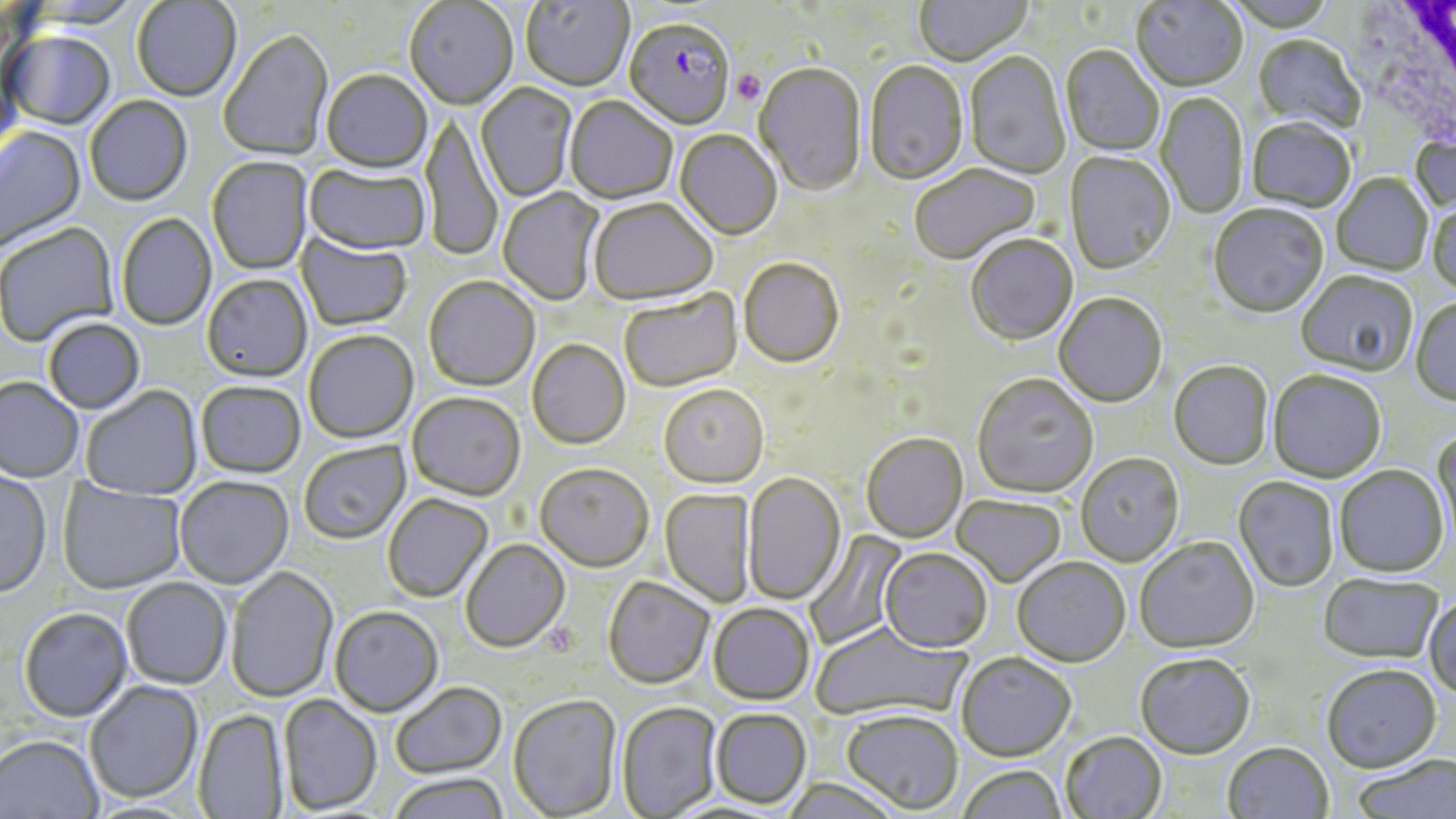

Approximate bounding boxes as named x1/y1/x2/y2 corners in pixels. White blood cell locations: (x1=1356, y1=0, x2=1456, y2=160). Plasmodium falciparum-infected red blood cell locations: (x1=624, y1=19, x2=735, y2=133). Uninfected red blood cell locations: (x1=521, y1=0, x2=633, y2=93), (x1=915, y1=0, x2=1032, y2=68), (x1=1131, y1=0, x2=1247, y2=93), (x1=132, y1=1, x2=242, y2=103), (x1=405, y1=1, x2=518, y2=111), (x1=218, y1=30, x2=334, y2=163), (x1=2, y1=32, x2=116, y2=132), (x1=1252, y1=36, x2=1365, y2=137), (x1=1061, y1=46, x2=1164, y2=157), (x1=964, y1=53, x2=1070, y2=180), (x1=864, y1=62, x2=968, y2=186), (x1=753, y1=64, x2=867, y2=198), (x1=321, y1=72, x2=433, y2=175), (x1=476, y1=84, x2=577, y2=203), (x1=1156, y1=92, x2=1248, y2=219), (x1=85, y1=97, x2=193, y2=208), (x1=565, y1=97, x2=677, y2=205), (x1=421, y1=112, x2=503, y2=263), (x1=1247, y1=120, x2=1355, y2=214), (x1=0, y1=125, x2=87, y2=255), (x1=674, y1=131, x2=782, y2=241), (x1=1410, y1=132, x2=1456, y2=216), (x1=1064, y1=152, x2=1175, y2=276), (x1=207, y1=157, x2=313, y2=276), (x1=304, y1=164, x2=431, y2=257), (x1=910, y1=165, x2=1041, y2=266), (x1=1332, y1=174, x2=1432, y2=276), (x1=497, y1=187, x2=605, y2=306), (x1=588, y1=199, x2=718, y2=308), (x1=1428, y1=200, x2=1456, y2=298), (x1=1209, y1=206, x2=1329, y2=320), (x1=116, y1=213, x2=217, y2=331), (x1=0, y1=223, x2=119, y2=348), (x1=296, y1=233, x2=412, y2=332), (x1=965, y1=236, x2=1078, y2=347), (x1=738, y1=260, x2=844, y2=370), (x1=1296, y1=272, x2=1418, y2=379), (x1=202, y1=274, x2=312, y2=383), (x1=424, y1=276, x2=540, y2=392), (x1=619, y1=290, x2=744, y2=393), (x1=1054, y1=294, x2=1167, y2=409), (x1=1410, y1=298, x2=1456, y2=408), (x1=43, y1=318, x2=145, y2=414), (x1=304, y1=330, x2=418, y2=444), (x1=527, y1=339, x2=630, y2=450), (x1=1168, y1=362, x2=1273, y2=472), (x1=1267, y1=372, x2=1386, y2=484), (x1=971, y1=376, x2=1098, y2=500), (x1=0, y1=377, x2=84, y2=484), (x1=196, y1=381, x2=306, y2=478), (x1=81, y1=386, x2=202, y2=501), (x1=659, y1=386, x2=769, y2=489), (x1=407, y1=392, x2=526, y2=501), (x1=1430, y1=426, x2=1456, y2=555), (x1=862, y1=434, x2=969, y2=544), (x1=298, y1=440, x2=410, y2=544), (x1=1076, y1=454, x2=1185, y2=568), (x1=534, y1=463, x2=654, y2=571), (x1=1334, y1=467, x2=1449, y2=580), (x1=0, y1=469, x2=52, y2=599), (x1=742, y1=473, x2=846, y2=606), (x1=174, y1=475, x2=294, y2=589), (x1=1233, y1=478, x2=1338, y2=593), (x1=58, y1=479, x2=187, y2=594), (x1=660, y1=489, x2=756, y2=608), (x1=383, y1=493, x2=493, y2=602), (x1=952, y1=496, x2=1066, y2=588), (x1=803, y1=528, x2=909, y2=651), (x1=1135, y1=538, x2=1260, y2=656), (x1=460, y1=539, x2=570, y2=653), (x1=880, y1=549, x2=992, y2=654), (x1=1012, y1=559, x2=1130, y2=669), (x1=226, y1=567, x2=338, y2=702), (x1=121, y1=577, x2=231, y2=690), (x1=602, y1=577, x2=714, y2=690), (x1=1318, y1=577, x2=1443, y2=665), (x1=1425, y1=597, x2=1456, y2=701), (x1=708, y1=604, x2=814, y2=706), (x1=330, y1=605, x2=444, y2=717), (x1=18, y1=607, x2=133, y2=721), (x1=810, y1=621, x2=970, y2=724), (x1=955, y1=654, x2=1076, y2=764), (x1=1135, y1=656, x2=1255, y2=762), (x1=1321, y1=667, x2=1441, y2=775), (x1=84, y1=681, x2=203, y2=803), (x1=390, y1=681, x2=507, y2=779), (x1=278, y1=693, x2=382, y2=815), (x1=508, y1=694, x2=622, y2=818), (x1=616, y1=702, x2=722, y2=818), (x1=193, y1=708, x2=288, y2=819), (x1=711, y1=709, x2=811, y2=809), (x1=841, y1=711, x2=963, y2=815), (x1=1060, y1=733, x2=1167, y2=819), (x1=0, y1=734, x2=103, y2=819), (x1=1222, y1=744, x2=1333, y2=819), (x1=1351, y1=755, x2=1456, y2=819), (x1=958, y1=766, x2=1066, y2=819), (x1=387, y1=772, x2=510, y2=819), (x1=783, y1=778, x2=902, y2=818). Platelet locations: (x1=732, y1=70, x2=767, y2=106). Slide-level diagnosis: Plasmodium falciparum. May-Grünwald-Giemsa-stained preparation. Captured at 1000x magnification. Optical microscopy. Image is 1456×819 pixels. Single field of view. Thin blood smear.